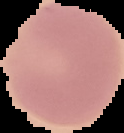

The area outside the segmented cell region is set to black. From a thin blood film. Result: negative for Plasmodium parasites. Image is 124×133 pixels.